Report the malaria status.
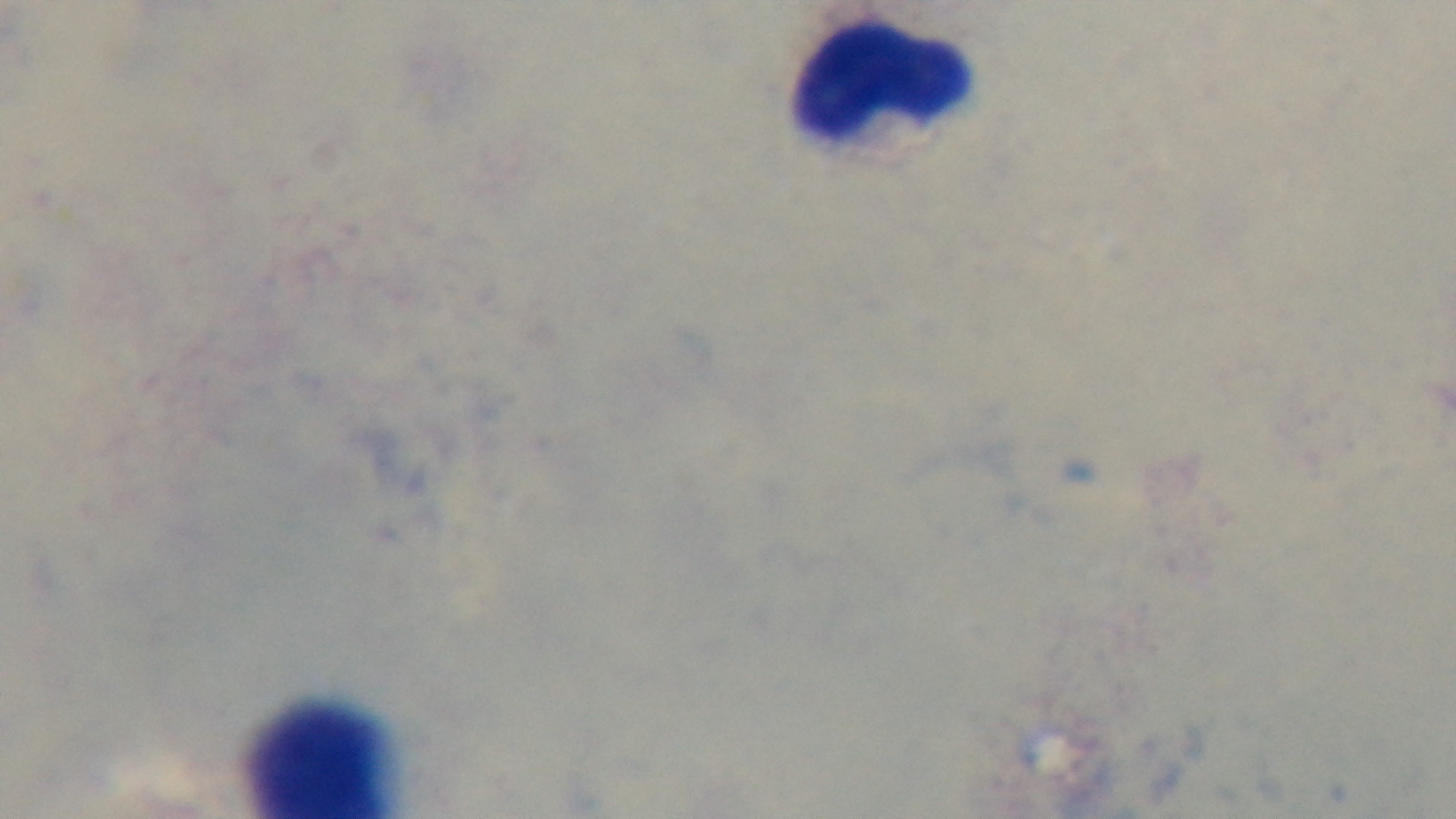
Uninfected.

capture = mounted 4K digital camera
stain = Giemsa
objective = 100x oil immersion
field of view = one from the slide
modality = light microscopy
preparation = thick blood film